State which parasite is depicted.
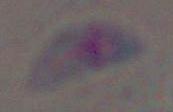

This is Toxoplasma gondii.

Captured at 1000x magnification. Micrograph.